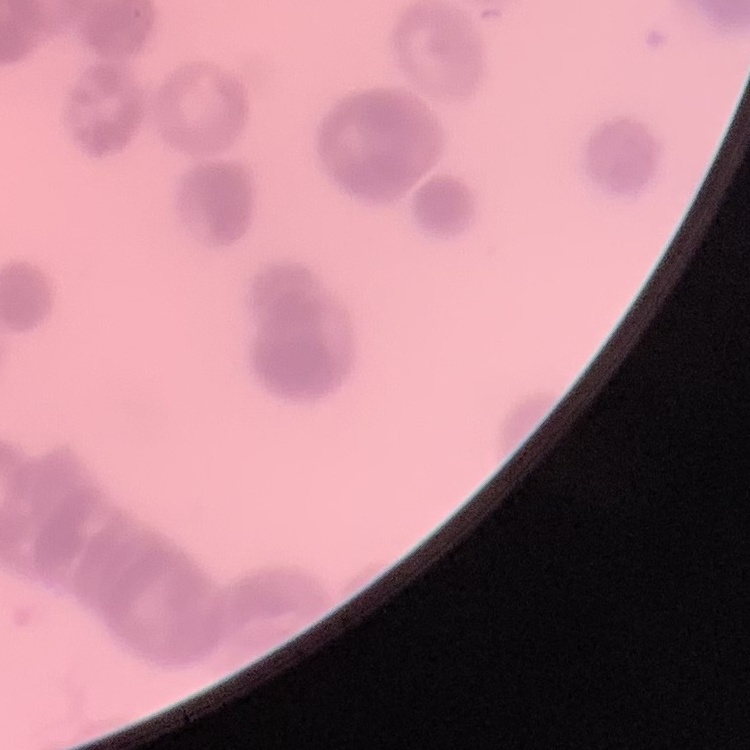
erythrocyte morphology = rouleaux formation
preparation = thin peripheral smear
stain = Field's or Giemsa
image type = one tile cut from a larger photomicrograph